Describe the morphology of the red blood cells.
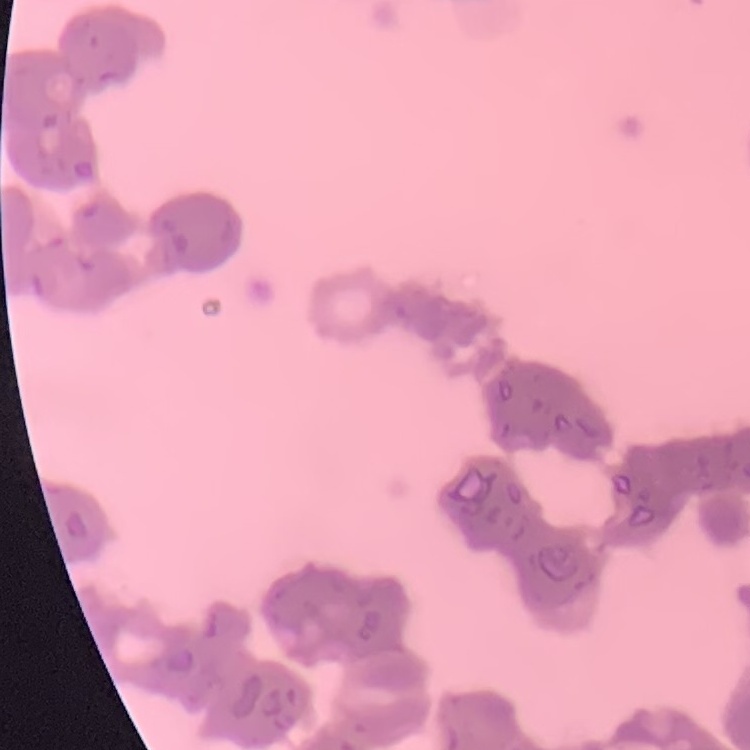
Rouleaux formation.

Summary:
  - Image type: one tile cut from a larger photomicrograph
  - Stain: Field's or Giemsa
  - Preparation: thin peripheral smear